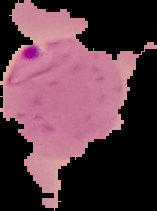 The area outside the segmented cell region is set to black. Malaria status: parasitized. From a thin blood film. Image is 157×211 pixels.